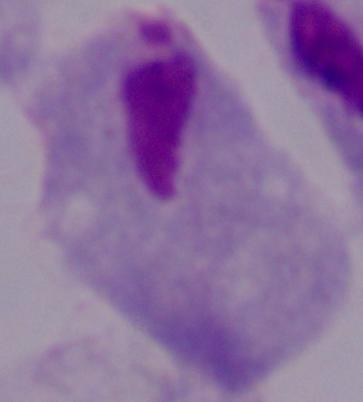

modality = photomicrograph
magnification = 1000x
identification = trichomonad